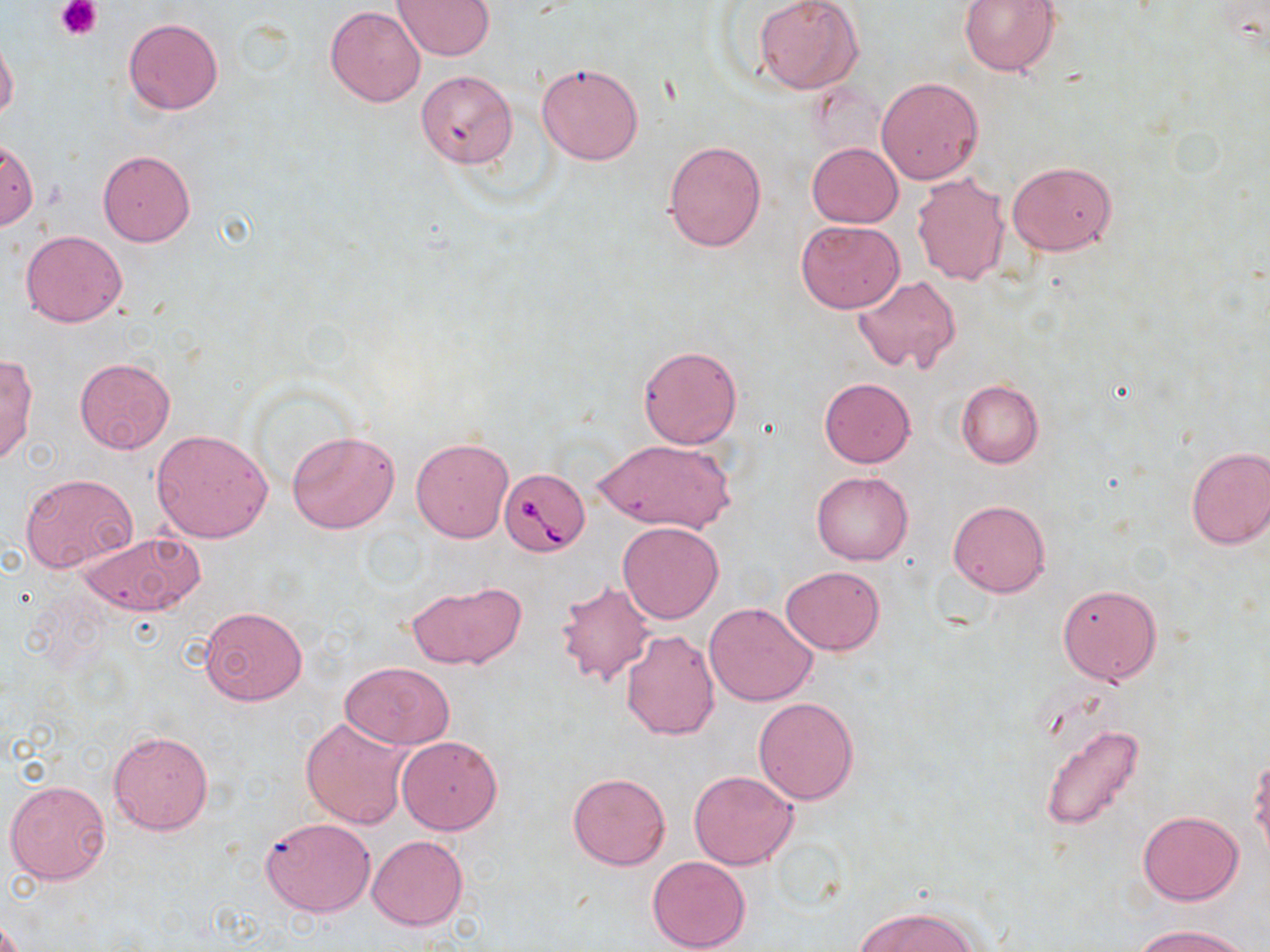

Approximate bounding boxes as (x1,y1)-(x2,y2) corner pairs in pixels. Uninfected red blood cell locations: (392,0)-(494,60), (754,0)-(862,95), (959,0)-(1061,76), (325,6)-(426,108), (124,17)-(223,114), (0,32)-(19,123), (536,60)-(644,165), (415,69)-(518,168), (876,77)-(984,185), (1,139)-(39,231), (662,139)-(767,252), (806,143)-(903,228), (97,150)-(195,247), (1008,161)-(1117,255), (911,172)-(1011,285), (796,220)-(905,313), (20,231)-(126,327), (851,275)-(962,375), (638,344)-(743,448), (0,354)-(38,467), (73,358)-(175,455), (819,377)-(915,468), (956,379)-(1044,469), (150,428)-(273,542), (286,429)-(401,534), (411,437)-(514,543), (592,437)-(735,535), (1184,445)-(1270,550), (812,471)-(913,566), (20,473)-(137,573), (949,500)-(1049,597), (618,521)-(723,623), (76,532)-(203,616), (780,564)-(885,656), (404,580)-(528,671), (554,580)-(658,688), (1058,584)-(1161,685), (705,601)-(818,707), (198,605)-(307,706), (621,629)-(719,740), (341,661)-(454,748), (754,697)-(858,805), (300,715)-(412,830), (1039,724)-(1147,831), (108,730)-(212,835), (396,736)-(502,834), (1250,763)-(1270,868), (688,771)-(798,870), (567,772)-(671,870), (4,778)-(113,885), (1138,810)-(1244,905), (261,817)-(376,918), (367,835)-(468,931), (647,856)-(750,952), (855,906)-(980,951), (1136,923)-(1251,952). Platelet locations: (54,0)-(102,41). Babesia divergens-infected red blood cell locations: (499,467)-(589,556). Slide-level diagnosis: Babesia divergens. Image is 1270×952 pixels. Thin blood film. Single field of view. Captured at 1000x magnification. Light microscopy. May-Grünwald-Giemsa-stained preparation.